Classify this cell by malaria status.
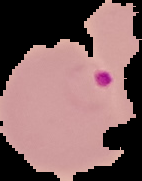

Parasitized.

preparation = thin blood smear
image type = segmented cell region on a black background
image size = 142×181 pixels